Assess this cell for malaria.
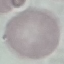

Uninfected.

Summary:
  - Stain: Giemsa
  - Image type: cell patch, automatically extracted from a larger field of view and resized to 64 × 64 pixels
  - Preparation: thin blood film
  - Capture: smartphone through the microscope eyepiece